Describe the morphology of the red blood cells.
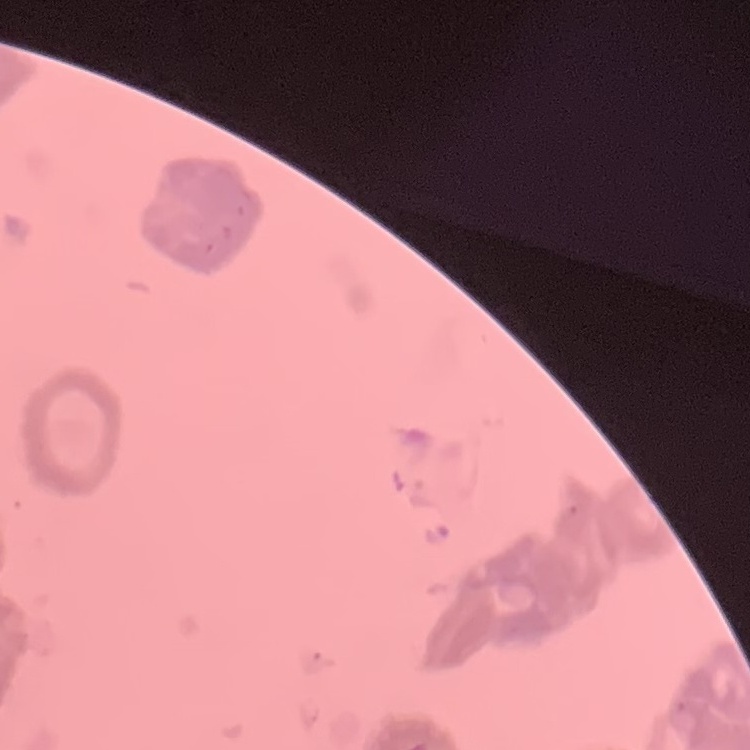

They show rouleaux formation.

image type = one tile cut from a larger photomicrograph
preparation = thin blood smear
stain = Field's or Giemsa